Locate every leukocyte (white blood cell).
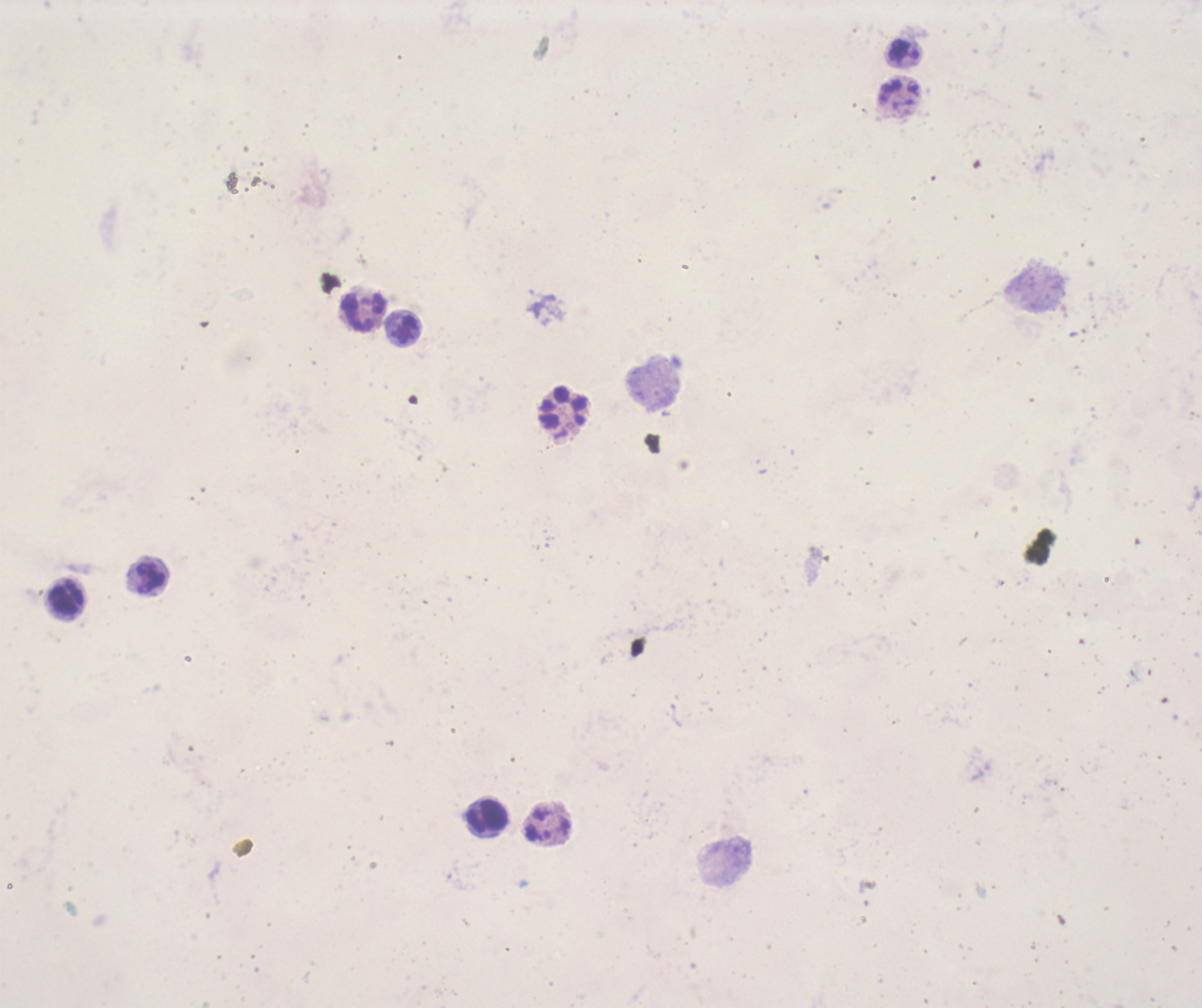

Approximate centers as [x, y] in pixels.
Leukocytes: [903, 52], [361, 311], [403, 328], [562, 409], [148, 576], [67, 600], [487, 820].

Image is 1202×1008 pixels. Result: no Plasmodium parasites detected. Thick smear of blood. Previously used in an actual diagnosis. Coloration quality: bad. One field from this slide. 100x magnification. Background quality: unsatisfactory. Romanowsky stain.